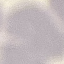
Result: negative for malaria parasites. Cell patch, automatically extracted from a larger field of view and resized to 64 × 64 pixels. Giemsa stain. Thin blood smear. Acquired by smartphone through the microscope eyepiece.